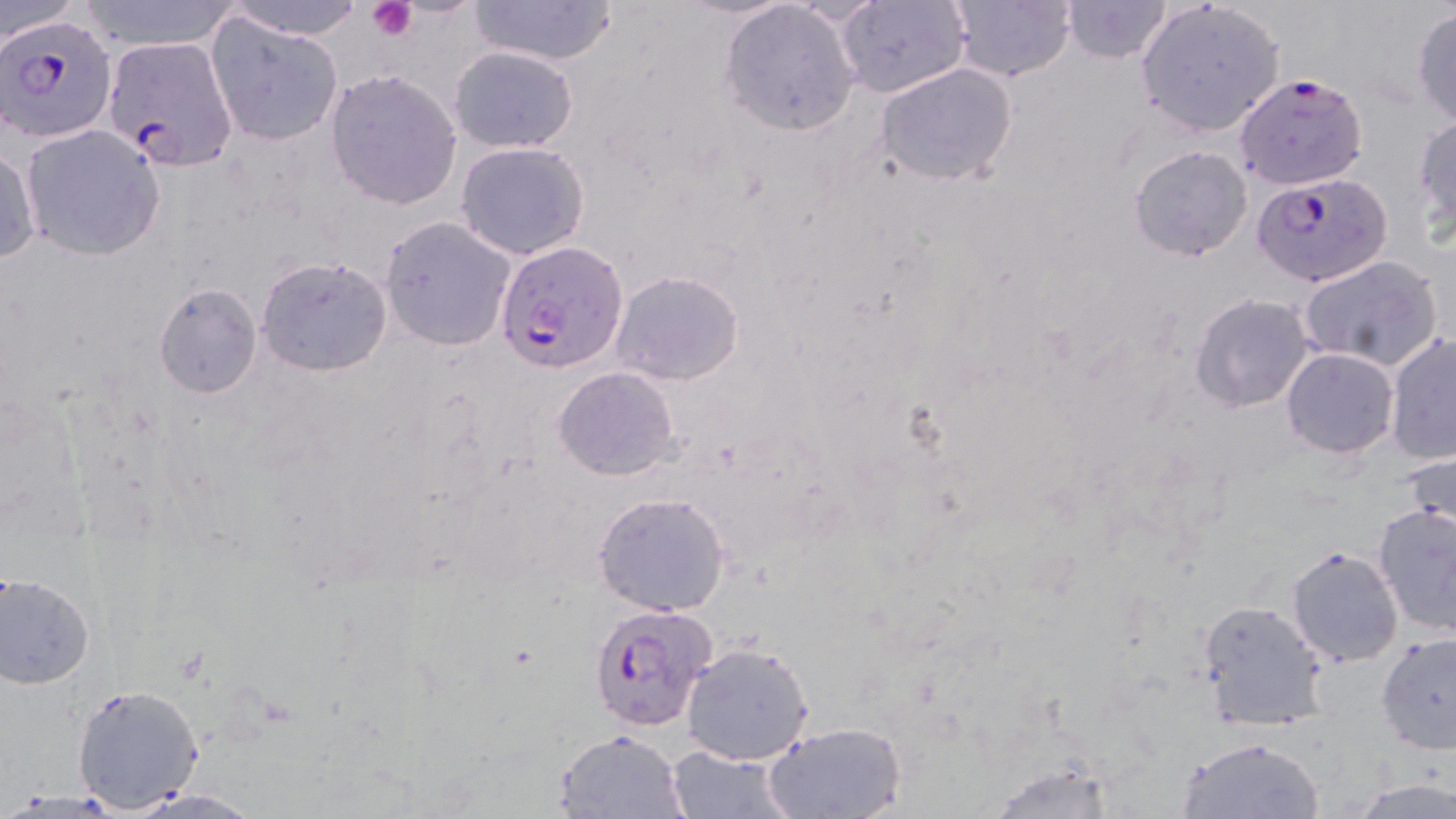

Approximate bounding boxes as (x1, y1, x2, y2) in pixels. Platelet locations: (368, 0, 418, 40). Uninfected red blood cell locations (subset): (76, 0, 243, 52), (219, 0, 367, 40), (463, 0, 621, 67), (946, 0, 1077, 83), (1062, 0, 1173, 63), (1135, 0, 1286, 139), (3, 1, 85, 44), (834, 1, 972, 99), (717, 2, 861, 137), (1409, 5, 1456, 128), (206, 16, 344, 144), (447, 45, 580, 154), (875, 62, 1021, 189), (324, 70, 462, 209), (1412, 112, 1456, 237), (20, 124, 166, 262), (455, 141, 590, 260), (0, 142, 41, 267), (1129, 143, 1252, 261), (379, 217, 517, 351), (1298, 254, 1445, 371), (255, 255, 393, 377), (609, 271, 745, 386), (154, 283, 261, 398), (1189, 293, 1314, 412), (1385, 332, 1455, 463), (1280, 346, 1398, 458), (553, 367, 679, 481), (1, 389, 86, 533), (1401, 448, 1456, 551), (590, 490, 735, 616), (1372, 501, 1455, 638), (1284, 544, 1404, 668), (1, 572, 96, 687), (1196, 599, 1329, 731), (1376, 632, 1456, 753), (681, 642, 815, 764), (71, 682, 205, 812), (761, 720, 907, 819), (553, 730, 689, 817), (1177, 735, 1325, 818), (664, 744, 797, 819), (982, 759, 1123, 818), (1352, 778, 1456, 817), (121, 788, 269, 817). Plasmodium falciparum-infected red blood cell locations (subset): (1, 14, 116, 142), (103, 36, 238, 170), (1235, 72, 1369, 189), (1251, 169, 1394, 288), (497, 240, 629, 373). Slide-level diagnosis: Plasmodium falciparum. 1000x magnification. Single field of view. May-Grünwald-Giemsa-stained preparation. Thin blood smear. Image is 1456×819 pixels. Optical microscopy.